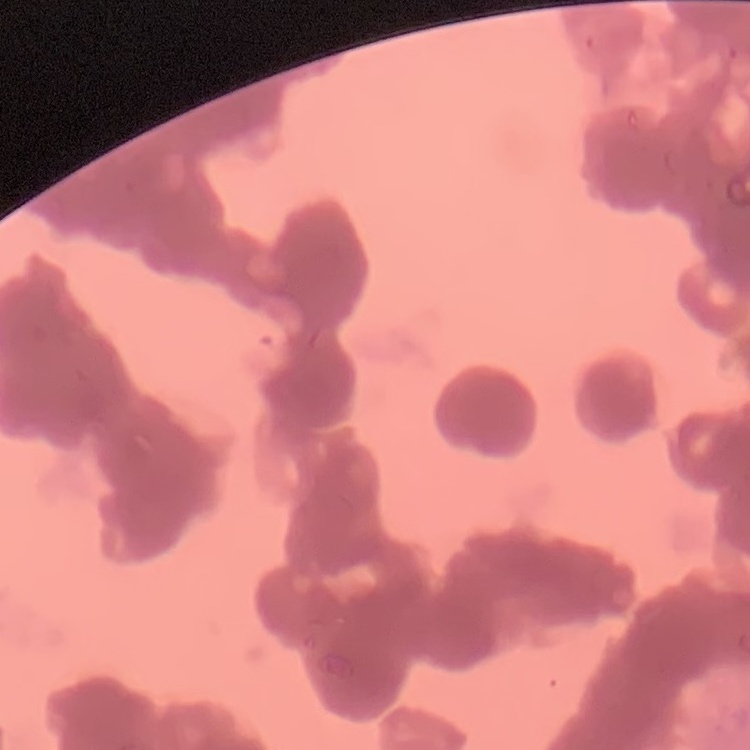

Summary:
  - Red blood cell morphology: rouleaux formation
  - Preparation: thin blood film
  - Image type: one tile cut from a larger photomicrograph
  - Stain: Field's or Giemsa